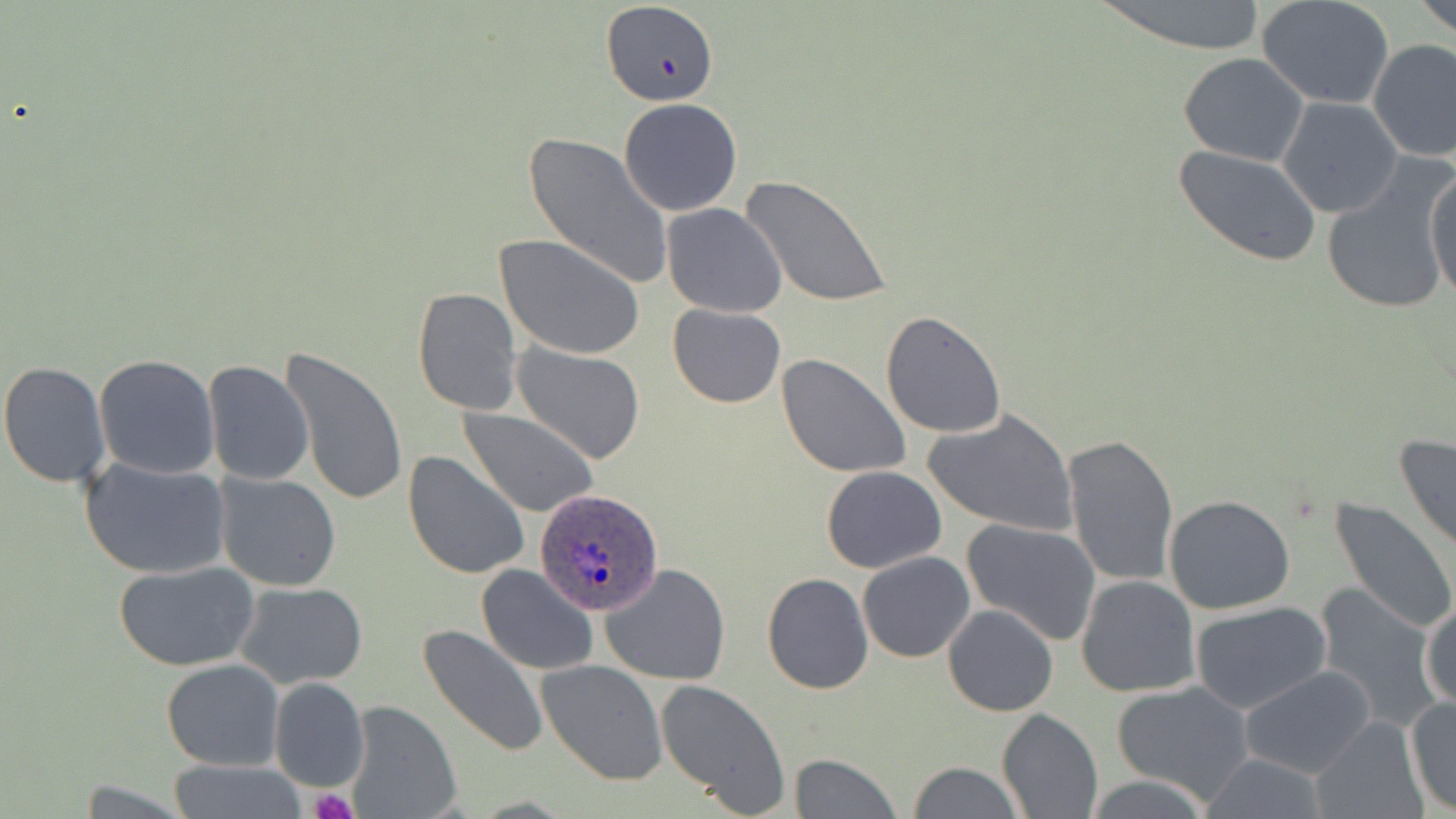

Summary:
  - Coordinate format: approximate bounding boxes as (x1, y1, x2, y2) in pixels
  - Plasmodium ovale-infected red blood cell locations: (536, 487, 664, 615)
  - Platelet locations: (311, 790, 355, 819)
  - Uninfected red blood cell locations: (1092, 0, 1272, 55), (1415, 0, 1456, 38), (1258, 1, 1395, 108), (601, 5, 720, 110), (1367, 38, 1455, 163), (1178, 53, 1310, 167), (1276, 96, 1404, 220), (619, 98, 743, 217), (524, 131, 675, 291), (1175, 144, 1322, 268), (1322, 158, 1455, 316), (1425, 163, 1456, 302), (741, 173, 891, 308), (660, 203, 787, 318), (496, 233, 645, 360), (412, 288, 522, 414), (668, 304, 785, 408), (880, 310, 1006, 438), (512, 341, 645, 463), (282, 349, 407, 507), (776, 352, 914, 479), (94, 354, 219, 478), (0, 359, 110, 489), (203, 359, 315, 486), (461, 408, 600, 519), (923, 409, 1078, 536), (1062, 433, 1179, 587), (1394, 433, 1456, 558), (403, 450, 529, 578), (79, 455, 232, 580), (821, 465, 947, 573), (215, 472, 340, 590), (1163, 495, 1296, 614), (1329, 498, 1456, 637), (962, 520, 1102, 646), (858, 551, 975, 662), (114, 560, 262, 671), (600, 563, 731, 684), (476, 564, 598, 675), (761, 571, 874, 694), (1075, 574, 1201, 698), (235, 581, 367, 689), (1312, 586, 1442, 731), (1420, 595, 1456, 711), (1190, 602, 1332, 714), (942, 604, 1059, 716), (420, 623, 548, 758), (161, 659, 285, 771), (538, 659, 668, 786), (1237, 665, 1377, 778), (268, 677, 368, 794), (654, 678, 792, 815), (1109, 680, 1257, 807), (1405, 695, 1456, 815), (344, 700, 460, 819), (997, 707, 1103, 819), (1309, 715, 1429, 819), (790, 755, 902, 818), (1195, 756, 1334, 817), (169, 758, 302, 818), (905, 761, 1023, 818), (1083, 774, 1216, 817), (69, 780, 198, 816)
  - Slide-level diagnosis: Plasmodium ovale
  - Preparation: thin blood film
  - Modality: optical microscopy
  - Stain: May-Grünwald-Giemsa
  - Field of view: single
  - Magnification: 1000x
  - Image size: 1456×819 pixels